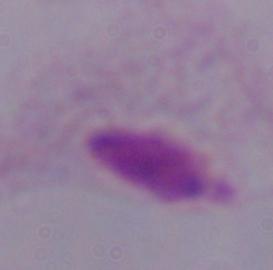
magnification: 1000x
modality: photomicrograph
identification: trichomonad